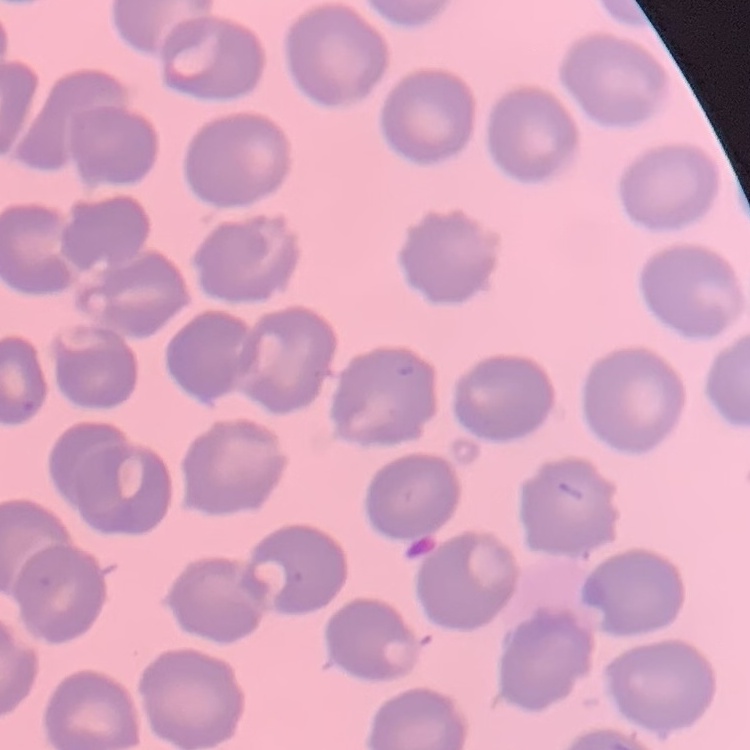

Summary:
  - Red blood cell morphology: no rouleaux formation
  - Preparation: thin blood film
  - Image type: square crop of a larger photomicrograph
  - Stain: Field's or Giemsa